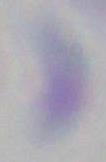

Toxoplasma gondii is shown. Photomicrograph. Captured at 1000x magnification.